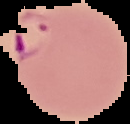

Image is 130×124 pixels. The area outside the segmented cell region is set to black. From a thin blood smear. Result: Plasmodium parasites identified.